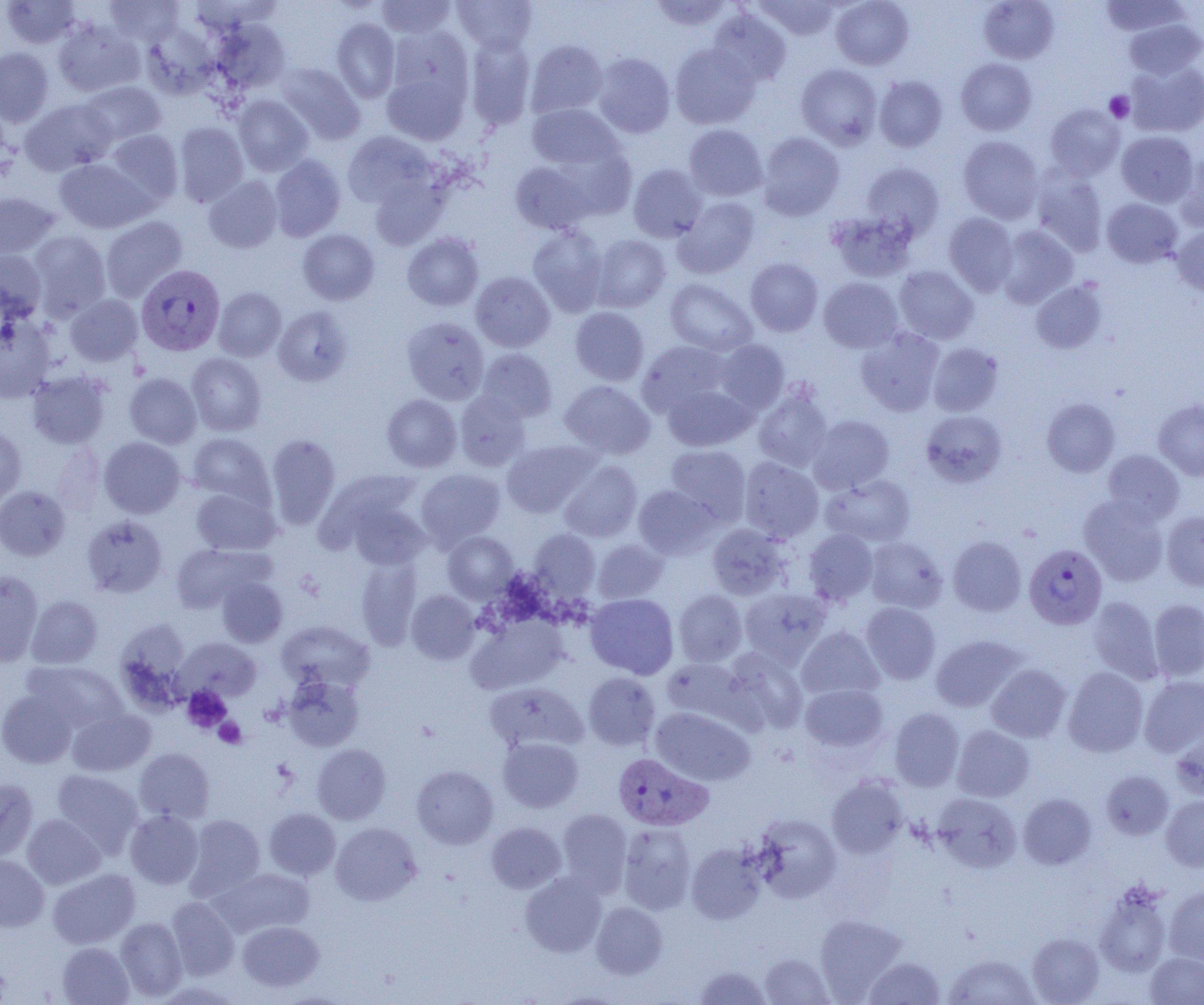
Summary:
  - Coordinate format: approximate bounding boxes as (x1, y1, x2, y2) in pixels
  - Uninfected red blood cell locations: (2, 0, 81, 48), (105, 0, 184, 47), (376, 0, 457, 39), (452, 0, 537, 53), (649, 0, 734, 31), (754, 0, 841, 41), (831, 0, 913, 70), (979, 0, 1059, 64), (1099, 0, 1190, 37), (708, 8, 791, 87), (331, 18, 400, 103), (1123, 18, 1204, 79), (53, 19, 144, 97), (211, 19, 290, 93), (141, 24, 218, 99), (386, 25, 474, 108), (465, 35, 536, 130), (525, 39, 608, 119), (670, 43, 760, 129), (0, 47, 54, 127), (592, 52, 676, 138), (956, 58, 1037, 135), (1126, 60, 1204, 137), (275, 63, 365, 144), (796, 63, 883, 149), (381, 72, 468, 145), (873, 75, 947, 152), (80, 81, 166, 146), (233, 95, 313, 176), (0, 97, 11, 173), (20, 98, 115, 175), (527, 103, 623, 171), (1045, 104, 1125, 179), (173, 122, 248, 207), (684, 124, 768, 201), (104, 129, 183, 207), (343, 131, 435, 209), (1116, 131, 1198, 207), (757, 132, 845, 220), (958, 135, 1044, 223), (1175, 154, 1204, 231), (269, 155, 345, 242), (55, 158, 153, 233), (509, 159, 599, 234), (863, 162, 944, 239), (628, 164, 707, 242), (1030, 167, 1109, 256), (203, 175, 283, 253), (369, 175, 451, 251), (0, 193, 58, 259), (674, 197, 759, 278), (1102, 198, 1183, 268), (827, 211, 917, 282), (943, 212, 1018, 296), (100, 216, 187, 302), (527, 225, 608, 316), (996, 226, 1078, 308), (1171, 226, 1204, 296), (298, 229, 379, 305), (28, 231, 111, 319), (402, 232, 483, 310), (590, 234, 671, 312), (0, 250, 47, 321), (746, 258, 823, 336), (893, 266, 979, 344), (471, 271, 555, 352), (819, 277, 903, 353), (665, 278, 757, 356), (1030, 280, 1107, 354), (213, 287, 286, 361), (64, 294, 143, 366), (273, 306, 352, 386), (570, 306, 649, 386), (0, 314, 55, 401), (402, 317, 489, 404), (856, 328, 944, 416), (637, 340, 731, 417), (715, 340, 789, 413), (927, 342, 1003, 416), (476, 348, 557, 423), (186, 353, 267, 436), (27, 370, 112, 449), (124, 373, 201, 449), (559, 380, 655, 459), (662, 384, 756, 451), (753, 384, 833, 472), (455, 391, 531, 471), (382, 394, 461, 472), (1042, 397, 1120, 477), (1153, 398, 1204, 480), (920, 410, 1007, 487), (807, 415, 894, 494), (0, 425, 26, 504), (187, 433, 274, 510), (266, 434, 341, 529), (99, 437, 185, 518), (502, 440, 597, 517), (50, 443, 106, 517), (665, 445, 751, 524), (1102, 450, 1184, 525), (738, 457, 823, 543), (559, 460, 642, 542), (416, 469, 505, 548), (327, 472, 427, 561), (821, 474, 915, 547), (634, 485, 719, 560), (0, 486, 70, 561), (191, 487, 280, 555), (1079, 496, 1169, 586), (1162, 511, 1204, 591), (82, 515, 168, 598), (707, 524, 791, 600), (529, 529, 600, 600), (804, 529, 878, 605), (443, 531, 517, 602), (948, 535, 1026, 616), (865, 537, 947, 613), (592, 539, 669, 603), (171, 543, 272, 614), (355, 556, 422, 650), (0, 570, 44, 666), (217, 577, 287, 647), (740, 587, 832, 668), (407, 590, 479, 664), (674, 590, 747, 667), (585, 594, 678, 678), (26, 595, 102, 668), (1088, 596, 1164, 684), (1149, 599, 1204, 681), (861, 602, 940, 684), (466, 615, 566, 693), (277, 621, 373, 690), (797, 626, 884, 700), (931, 635, 1025, 712), (176, 637, 261, 702), (724, 647, 807, 734), (661, 658, 758, 731), (22, 661, 127, 733), (986, 664, 1071, 742), (1063, 666, 1149, 757), (583, 672, 660, 750), (282, 674, 365, 752), (1139, 675, 1204, 757), (484, 681, 588, 753), (800, 684, 888, 752), (0, 688, 79, 768), (67, 707, 155, 777), (650, 707, 755, 786), (890, 708, 964, 791), (952, 725, 1035, 802), (1171, 731, 1204, 800), (498, 736, 584, 813), (312, 744, 391, 825), (135, 748, 215, 823), (411, 765, 498, 848), (52, 770, 144, 856), (1100, 770, 1173, 839), (826, 777, 907, 859), (0, 778, 39, 863), (933, 793, 1021, 872), (1018, 793, 1097, 869), (1161, 795, 1204, 871), (264, 808, 341, 879), (557, 809, 632, 896), (125, 810, 203, 888), (22, 814, 105, 888), (184, 814, 265, 900), (752, 814, 842, 903), (331, 822, 422, 905), (486, 822, 566, 894), (618, 824, 697, 915), (686, 843, 767, 924), (0, 854, 49, 931), (212, 867, 315, 937), (48, 869, 140, 949), (520, 872, 606, 957), (1094, 882, 1173, 977), (1164, 885, 1204, 966), (167, 897, 239, 980), (591, 902, 667, 978), (815, 914, 906, 1001), (115, 917, 187, 1001), (238, 921, 324, 991), (1027, 932, 1104, 1004), (57, 942, 134, 1005), (1144, 951, 1204, 1004), (759, 952, 834, 1005), (943, 953, 1040, 1005), (863, 956, 945, 1005), (693, 965, 772, 1004)
  - Plasmodium vivax-infected red blood cell locations: (136, 265, 225, 356), (1024, 543, 1107, 629), (613, 753, 712, 832)
  - Platelet locations: (1104, 91, 1134, 123), (182, 686, 231, 732), (214, 717, 246, 748)
  - Slide-level diagnosis: Plasmodium vivax
  - Modality: optical microscopy
  - Image size: 1204×1005 pixels
  - Preparation: thin blood film
  - Magnification: 1000x
  - Field of view: one of a larger specimen